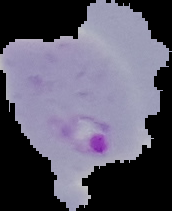
Image is 172×211 pixels. From a thin blood film. Segmented cell region on a black background. Malaria status: parasitized.